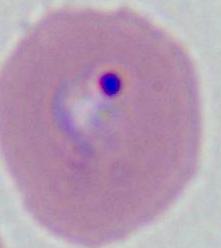

Micrograph. 400x or 1000x magnification. A Plasmodium parasite is seen.